Classify this cell by malaria status.
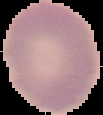
It is uninfected.

preparation: thin blood film
image_type: segmented cell region with the area outside set to black
image_size: 103×115 pixels